Assess the morphology of the erythrocytes.
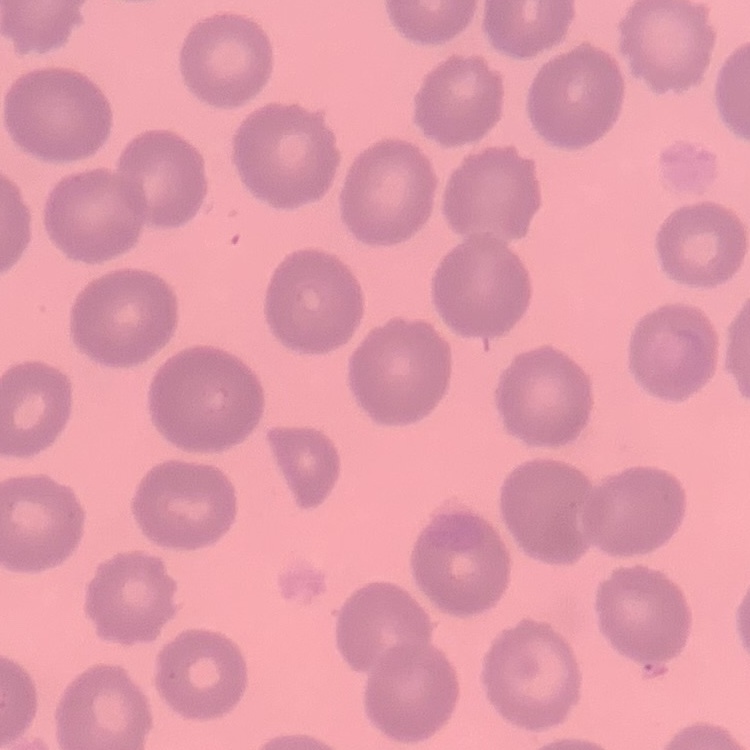

No rouleaux formation.

{
  "preparation": "thin blood film",
  "image_type": "one tile cut from a larger photomicrograph",
  "stain": "Field's or Giemsa"
}